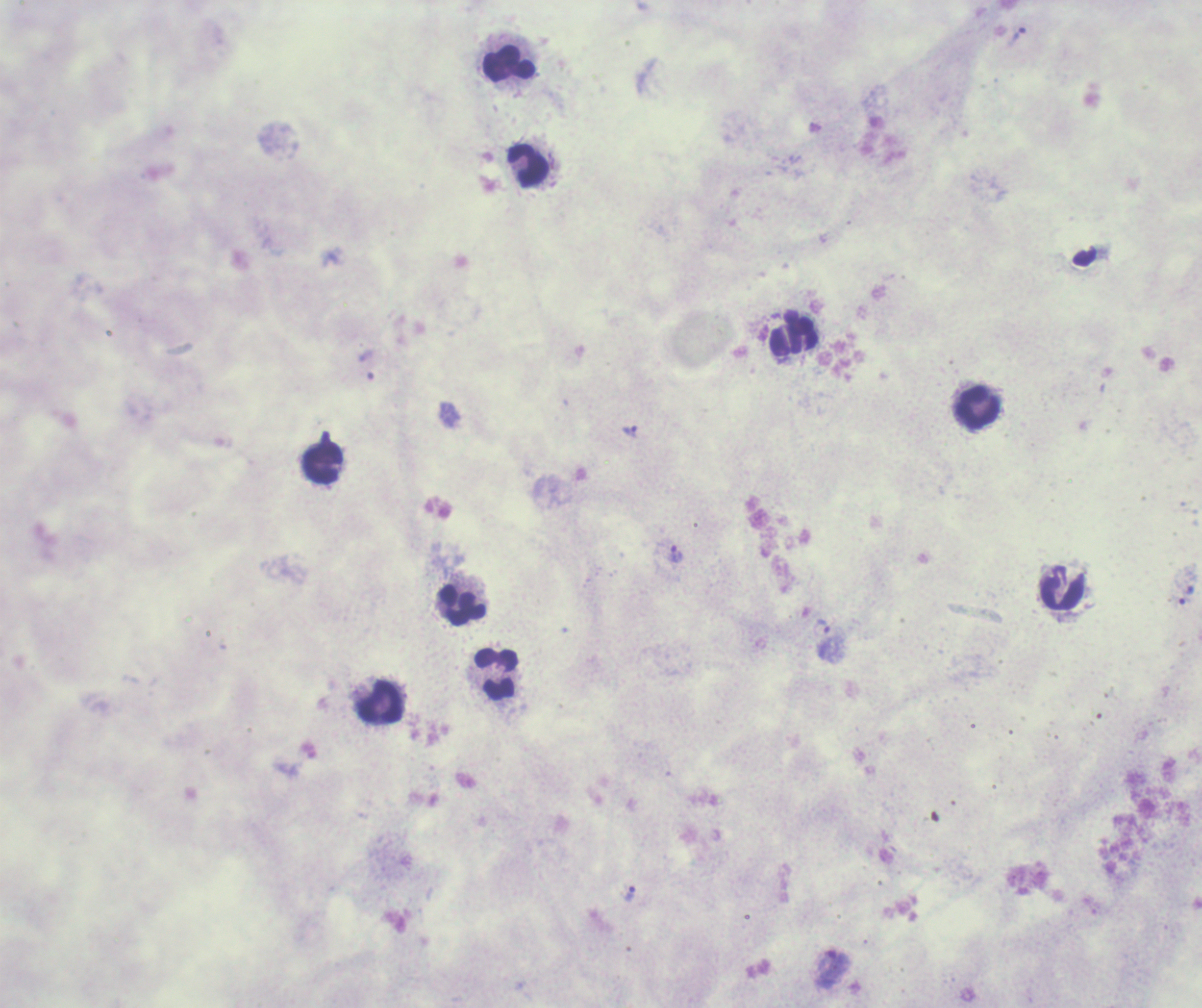
coordinate format = approximate centers as [x, y] in pixels
trophozoite locations = [1018, 37], [630, 431], [675, 554], [1186, 595], [821, 628], [629, 893], [831, 967]
leukocyte locations = [509, 66], [528, 167], [792, 338], [977, 409], [322, 462], [1061, 589], [460, 604], [495, 673], [379, 703]
image size = 1202×1008 pixels
magnification = 100x
background quality = poor
context = previously used in an actual diagnosis
result = malaria parasites identified
preparation = thick smear of blood
stain = Romanowsky
field of view = one from this slide